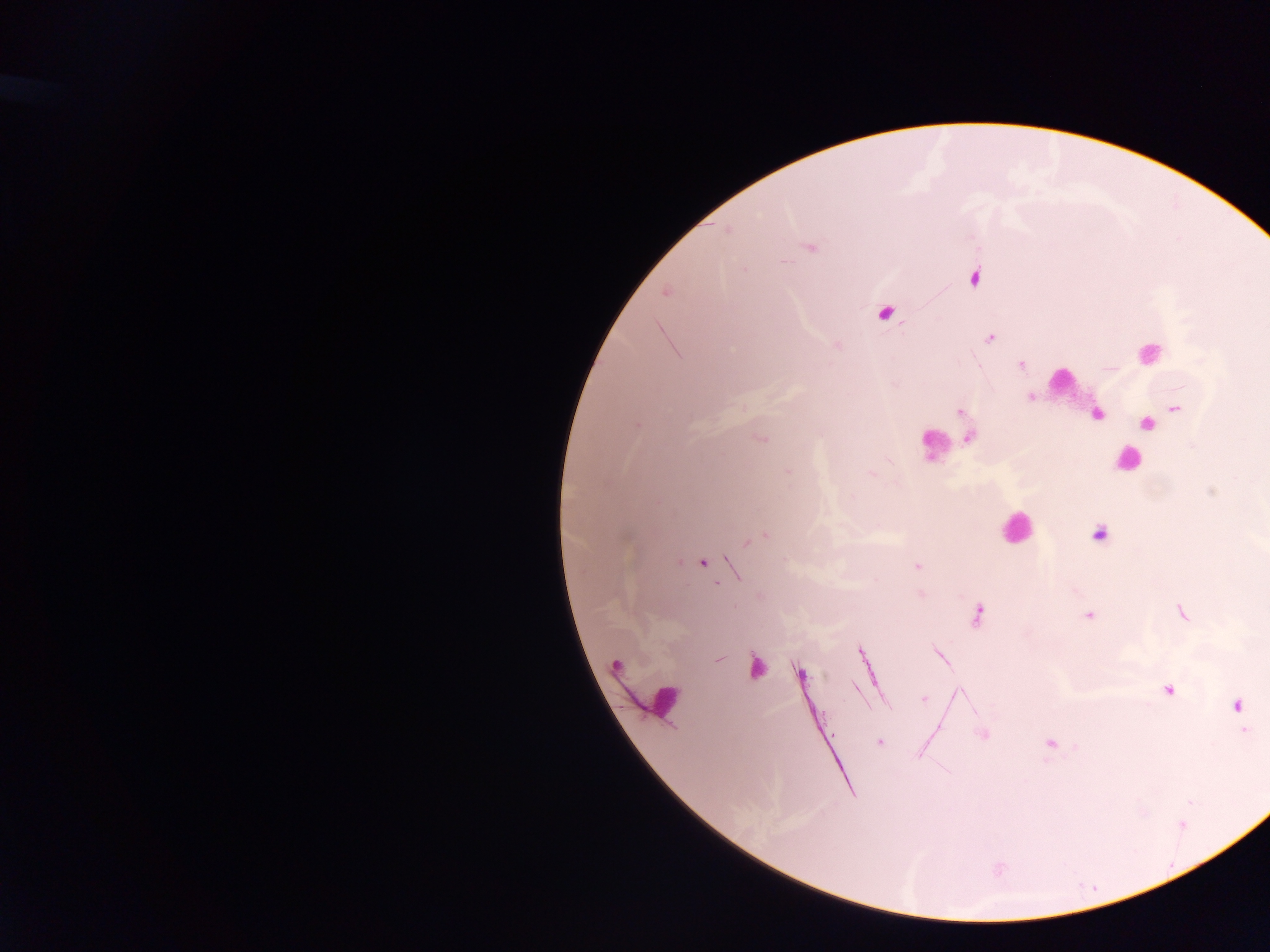

field of view = single
image size = 1270×952 pixels
leukocyte locations = approximate centers as {x, y} in pixels: {1147, 353}, {1060, 380}, {933, 444}, {1128, 460}, {1016, 528}, {756, 667}, {665, 702}
capture = mobile-phone photograph through a microscope
Plasmodium parasite locations = approximate centers as {x, y} in pixels: {727, 230}, {809, 247}, {973, 276}, {667, 291}, {885, 312}, {990, 337}, {836, 345}, {1020, 364}, {1030, 397}, {1174, 408}, {960, 411}, {1096, 415}, {1146, 423}, {636, 424}, {967, 437}, {760, 438}, {787, 472}, {869, 472}, {1098, 534}, {765, 535}, {747, 541}, {702, 562}, {916, 565}, {735, 572}, {921, 594}, {1181, 612}, {978, 614}, {1089, 615}, {861, 653}, {940, 654}, {718, 659}, {615, 666}, {798, 674}, {856, 688}, {1168, 688}, {959, 694}, {924, 699}, {1236, 705}, {1243, 730}, {983, 734}, {879, 741}, {1051, 742}
preparation = thick blood film
country = Ghana